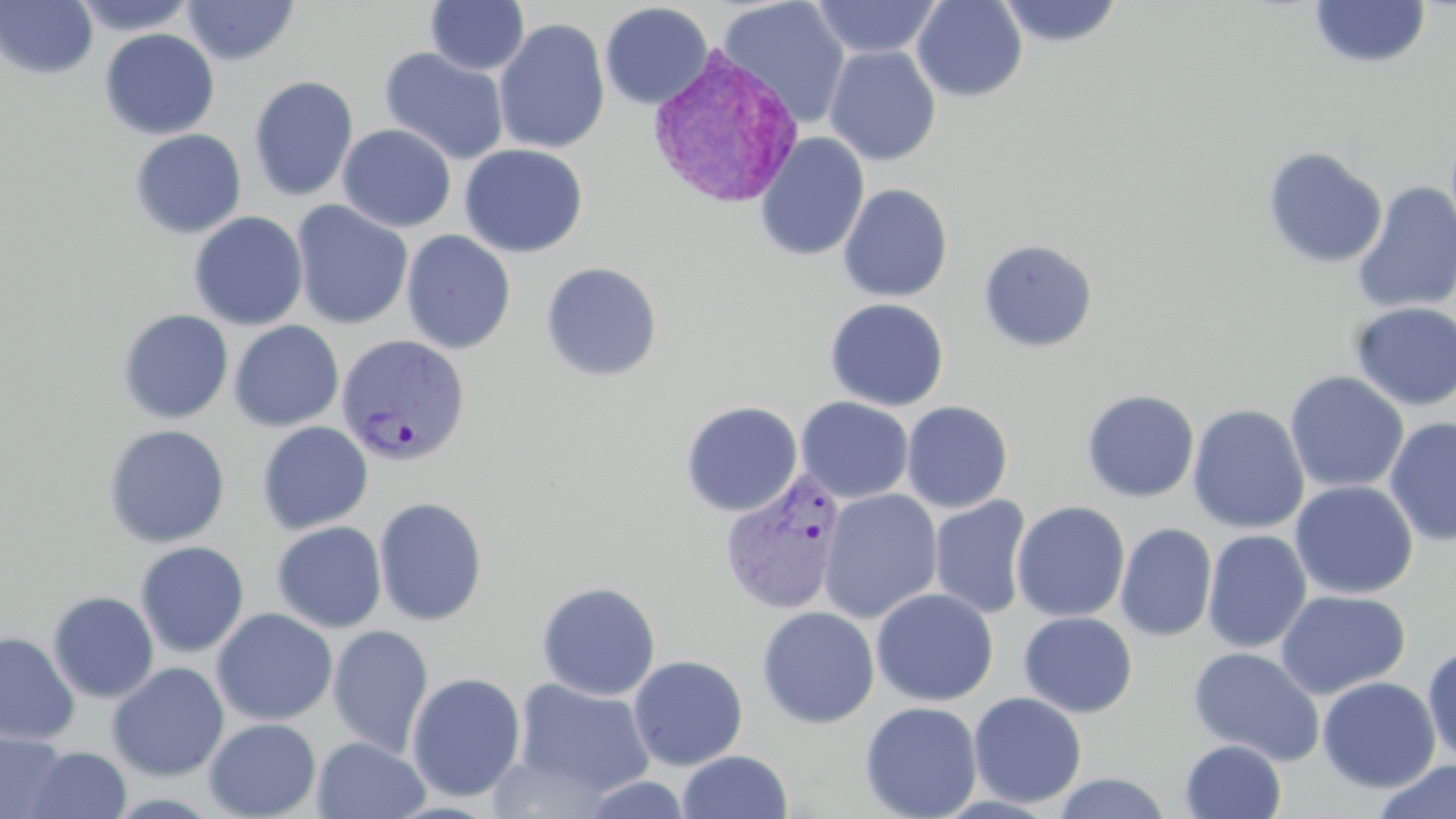

Summary:
  - Coordinate format: approximate bounding boxes as named x1/y1/x2/y2 corners in pixels
  - Plasmodium vivax-infected red blood cell locations: (x1=644, y1=44, x2=804, y2=211), (x1=335, y1=334, x2=470, y2=465), (x1=718, y1=470, x2=847, y2=616)
  - Uninfected red blood cell locations: (x1=0, y1=0, x2=98, y2=79), (x1=70, y1=0, x2=198, y2=36), (x1=181, y1=0, x2=300, y2=66), (x1=425, y1=0, x2=529, y2=75), (x1=717, y1=0, x2=851, y2=129), (x1=811, y1=0, x2=942, y2=59), (x1=912, y1=0, x2=1027, y2=102), (x1=996, y1=0, x2=1125, y2=48), (x1=1309, y1=1, x2=1431, y2=70), (x1=599, y1=2, x2=714, y2=110), (x1=494, y1=18, x2=610, y2=155), (x1=99, y1=28, x2=220, y2=140), (x1=824, y1=45, x2=941, y2=166), (x1=378, y1=47, x2=510, y2=166), (x1=248, y1=75, x2=359, y2=202), (x1=338, y1=124, x2=456, y2=232), (x1=129, y1=129, x2=246, y2=239), (x1=755, y1=132, x2=870, y2=262), (x1=459, y1=143, x2=589, y2=258), (x1=1262, y1=147, x2=1388, y2=269), (x1=1352, y1=181, x2=1456, y2=314), (x1=838, y1=183, x2=953, y2=302), (x1=290, y1=200, x2=413, y2=330), (x1=189, y1=211, x2=308, y2=330), (x1=401, y1=230, x2=517, y2=354), (x1=977, y1=238, x2=1099, y2=353), (x1=540, y1=261, x2=663, y2=382), (x1=824, y1=298, x2=950, y2=411), (x1=1349, y1=301, x2=1456, y2=412), (x1=117, y1=309, x2=233, y2=424), (x1=229, y1=320, x2=345, y2=432), (x1=1284, y1=370, x2=1409, y2=494), (x1=1081, y1=389, x2=1200, y2=503), (x1=795, y1=396, x2=914, y2=503), (x1=901, y1=400, x2=1013, y2=513), (x1=680, y1=401, x2=803, y2=517), (x1=1188, y1=404, x2=1309, y2=534), (x1=1384, y1=417, x2=1456, y2=545), (x1=256, y1=421, x2=373, y2=535), (x1=103, y1=424, x2=230, y2=548), (x1=1289, y1=480, x2=1419, y2=600), (x1=819, y1=489, x2=943, y2=624), (x1=929, y1=495, x2=1031, y2=620), (x1=373, y1=496, x2=488, y2=626), (x1=1011, y1=500, x2=1130, y2=622), (x1=271, y1=521, x2=387, y2=633), (x1=1115, y1=522, x2=1217, y2=642), (x1=1203, y1=530, x2=1312, y2=653), (x1=135, y1=541, x2=250, y2=658), (x1=536, y1=580, x2=661, y2=700), (x1=871, y1=588, x2=998, y2=706), (x1=1275, y1=589, x2=1411, y2=699), (x1=47, y1=591, x2=159, y2=703), (x1=756, y1=606, x2=879, y2=728), (x1=211, y1=608, x2=337, y2=726), (x1=1019, y1=611, x2=1138, y2=717), (x1=327, y1=624, x2=433, y2=759), (x1=0, y1=632, x2=80, y2=746), (x1=1422, y1=642, x2=1456, y2=764), (x1=1187, y1=646, x2=1325, y2=765), (x1=628, y1=654, x2=748, y2=770), (x1=106, y1=662, x2=229, y2=781), (x1=406, y1=672, x2=526, y2=802), (x1=508, y1=676, x2=657, y2=801), (x1=1317, y1=676, x2=1441, y2=793), (x1=968, y1=691, x2=1087, y2=808), (x1=860, y1=701, x2=983, y2=819), (x1=203, y1=717, x2=321, y2=819), (x1=0, y1=731, x2=70, y2=819), (x1=311, y1=736, x2=430, y2=819), (x1=1179, y1=739, x2=1287, y2=819), (x1=23, y1=746, x2=132, y2=818), (x1=676, y1=750, x2=793, y2=818), (x1=1372, y1=760, x2=1456, y2=819), (x1=1051, y1=772, x2=1173, y2=818), (x1=575, y1=773, x2=695, y2=819)
  - Slide-level diagnosis: Plasmodium vivax
  - Preparation: thin blood smear
  - Magnification: 1000x
  - Field of view: one of a larger specimen
  - Modality: optical microscopy
  - Image size: 1456×819 pixels
  - Stain: May-Grünwald-Giemsa